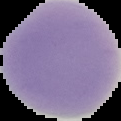
Summary:
  - Image size: 121×121 pixels
  - Result: no malaria parasites seen
  - Preparation: thin blood smear
  - Image type: segmented cell region on a black background